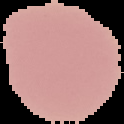
Summary:
  - Image size: 124×124 pixels
  - Malaria status: uninfected
  - Image type: segmented cell region with the area outside set to black
  - Preparation: thin blood smear